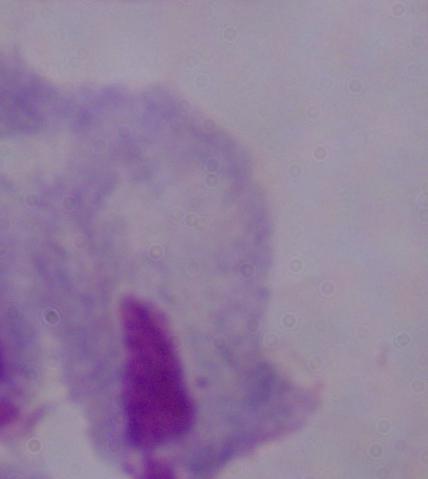

Photomicrograph. 1000x magnification. A trichomonad is seen.